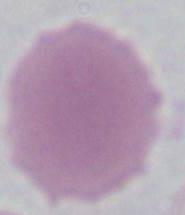
An erythrocyte is seen. Captured at 1000x magnification. Photomicrograph.